Name the parasite shown.
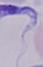
A trypanosome.

magnification = 1000x
modality = photomicrograph